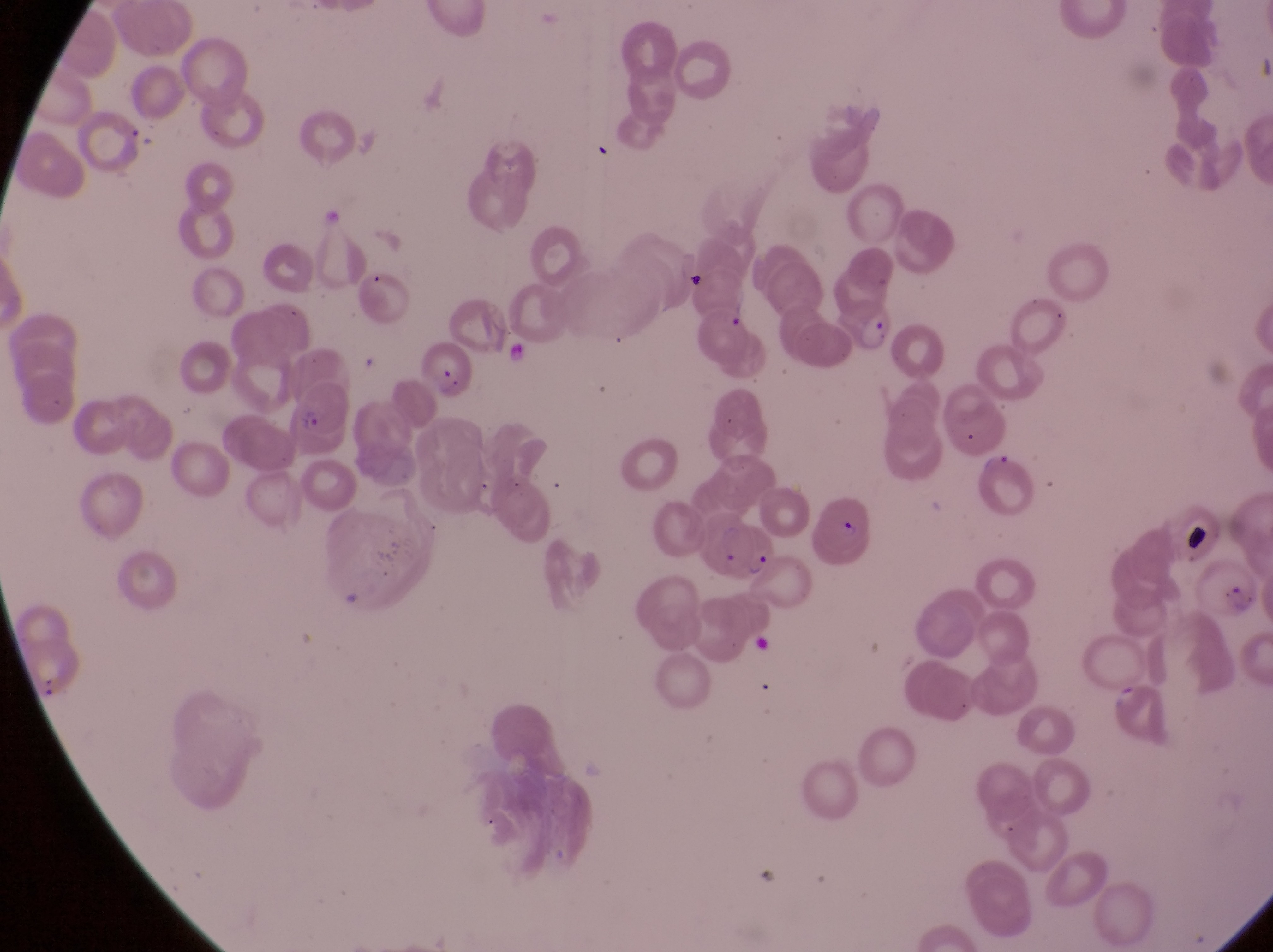

Approximate bounding boxes as {left, top, right, bottom} in pixels. Artifact (platelet-like body, stain precipitate, or debris) locations: {419, 340, 472, 402}, {1185, 521, 1217, 561}. Parasitised red blood cell locations: {845, 299, 898, 354}, {284, 380, 358, 457}, {814, 494, 881, 571}, {706, 507, 773, 577}. Image is 1273×952 pixels. Magnification of 1000x. Sample from Uganda. Thin blood film. One field of view. Captured by a smartphone held over the eyepiece of an Olympus CX-23 microscope.